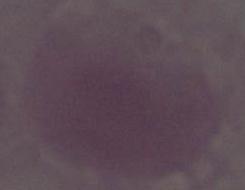
Summary:
  - Identification: erythrocyte
  - Modality: photomicrograph
  - Magnification: 1000x